Report the malaria status of this cell.
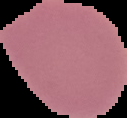
Uninfected.

{
  "preparation": "thin blood film",
  "image_size": "127×118 pixels",
  "image_type": "cell region segmented out of the field of view; surrounding area masked to black"
}